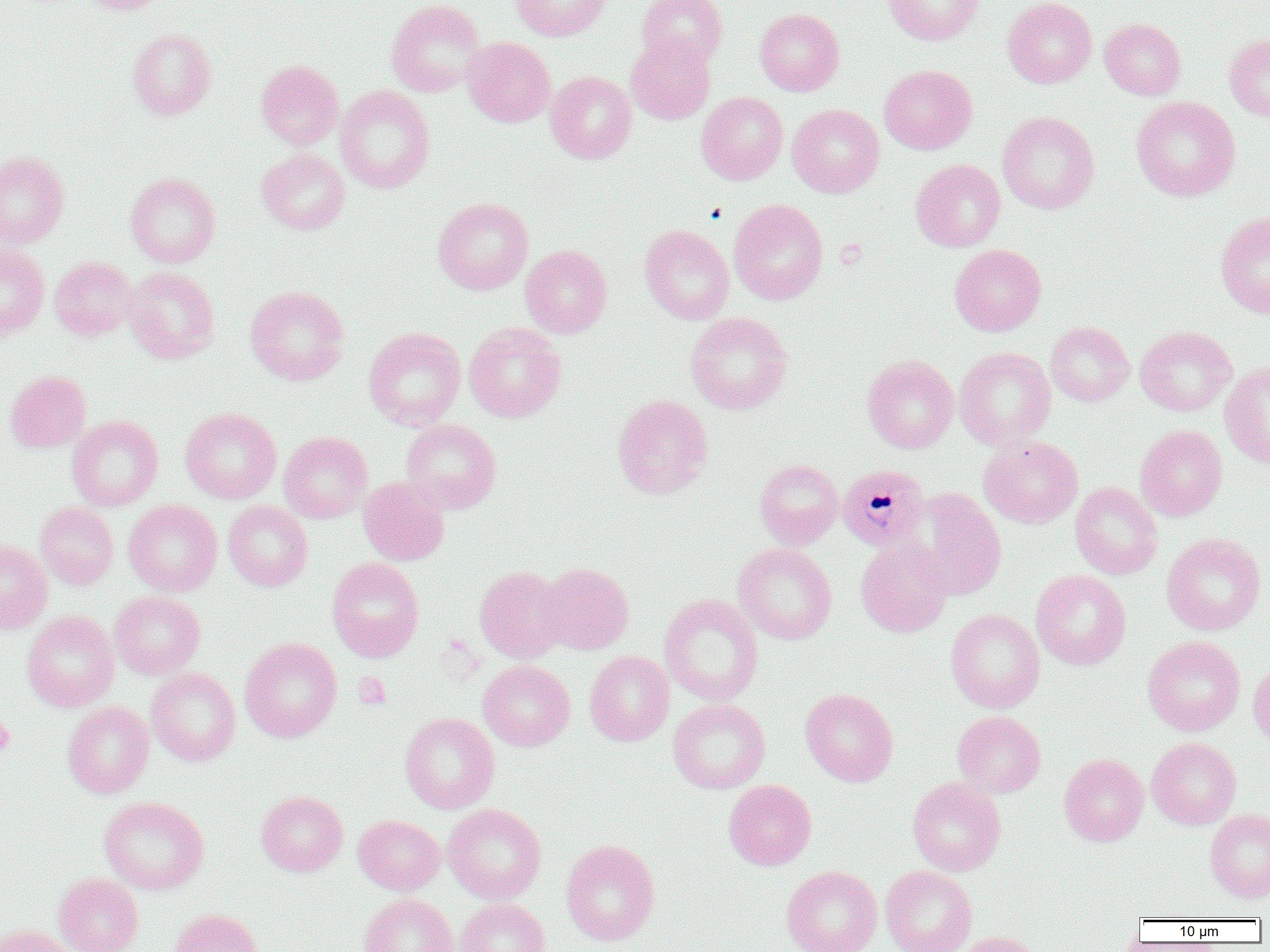

Approximate bounding boxes as (x1,y1)-(x2,y2) corner pairs in pixels. Plasmodium malariae-infected red blood cell locations: (837,465)-(929,550). Platelet locations: (353,672)-(392,709), (0,714)-(15,756). Uninfected red blood cell locations: (77,0)-(169,14), (386,0)-(486,97), (511,0)-(612,41), (637,0)-(727,68), (883,0)-(984,45), (1003,0)-(1097,88), (755,8)-(844,96), (1100,18)-(1185,99), (127,28)-(216,120), (1224,34)-(1270,121), (626,35)-(715,125), (461,37)-(556,127), (256,60)-(343,150), (879,64)-(977,154), (545,70)-(636,164), (335,85)-(435,194), (696,91)-(788,184), (1131,96)-(1240,201), (787,104)-(884,198), (997,111)-(1099,214), (257,148)-(350,235), (0,150)-(69,248), (910,159)-(1005,251), (125,172)-(220,268), (433,197)-(533,295), (729,199)-(828,305), (1215,211)-(1270,318), (639,224)-(734,324), (0,244)-(49,338), (949,244)-(1046,336), (520,245)-(612,338), (50,257)-(137,340), (124,267)-(220,364), (245,285)-(349,385), (685,312)-(793,414), (1045,321)-(1134,406), (464,322)-(566,423), (1135,325)-(1236,416), (364,327)-(466,430), (954,347)-(1056,450), (862,354)-(959,453), (1220,362)-(1270,468), (5,370)-(91,453), (612,394)-(713,500), (180,407)-(281,504), (67,416)-(163,511), (401,419)-(501,514), (1135,424)-(1227,521), (278,431)-(373,523), (979,435)-(1083,528), (754,459)-(843,549), (358,477)-(449,565), (1070,482)-(1162,580), (911,490)-(1006,600), (123,499)-(222,596), (223,500)-(312,591), (35,502)-(119,589), (1162,533)-(1266,635), (856,535)-(953,637), (0,540)-(52,634), (733,543)-(837,645), (327,557)-(424,662), (536,562)-(634,655), (474,565)-(567,663), (1031,569)-(1131,669), (110,590)-(205,679), (659,593)-(763,706), (945,608)-(1045,713), (22,610)-(119,712), (1142,635)-(1245,736), (240,637)-(342,742), (585,650)-(674,746), (1249,658)-(1270,749), (478,659)-(575,751), (146,667)-(241,766), (800,688)-(898,786), (667,698)-(770,794), (62,702)-(154,798), (953,711)-(1046,798), (399,712)-(500,813), (1147,737)-(1241,829), (1059,753)-(1149,846), (907,776)-(1006,876), (723,779)-(817,870), (256,790)-(348,876), (99,796)-(209,895), (442,803)-(546,904), (1204,808)-(1270,902), (353,815)-(445,895), (560,838)-(661,945), (782,865)-(882,952), (880,865)-(977,952), (53,873)-(144,952), (359,893)-(458,952), (455,898)-(550,952), (169,908)-(265,952), (1,925)-(78,952), (954,931)-(1042,952). Slide-level diagnosis: Plasmodium malariae. Single field of view. Optical microscopy. Image is 1270×952 pixels. Thin blood film. 1000x magnification.